Locate every leukocyte (white blood cell).
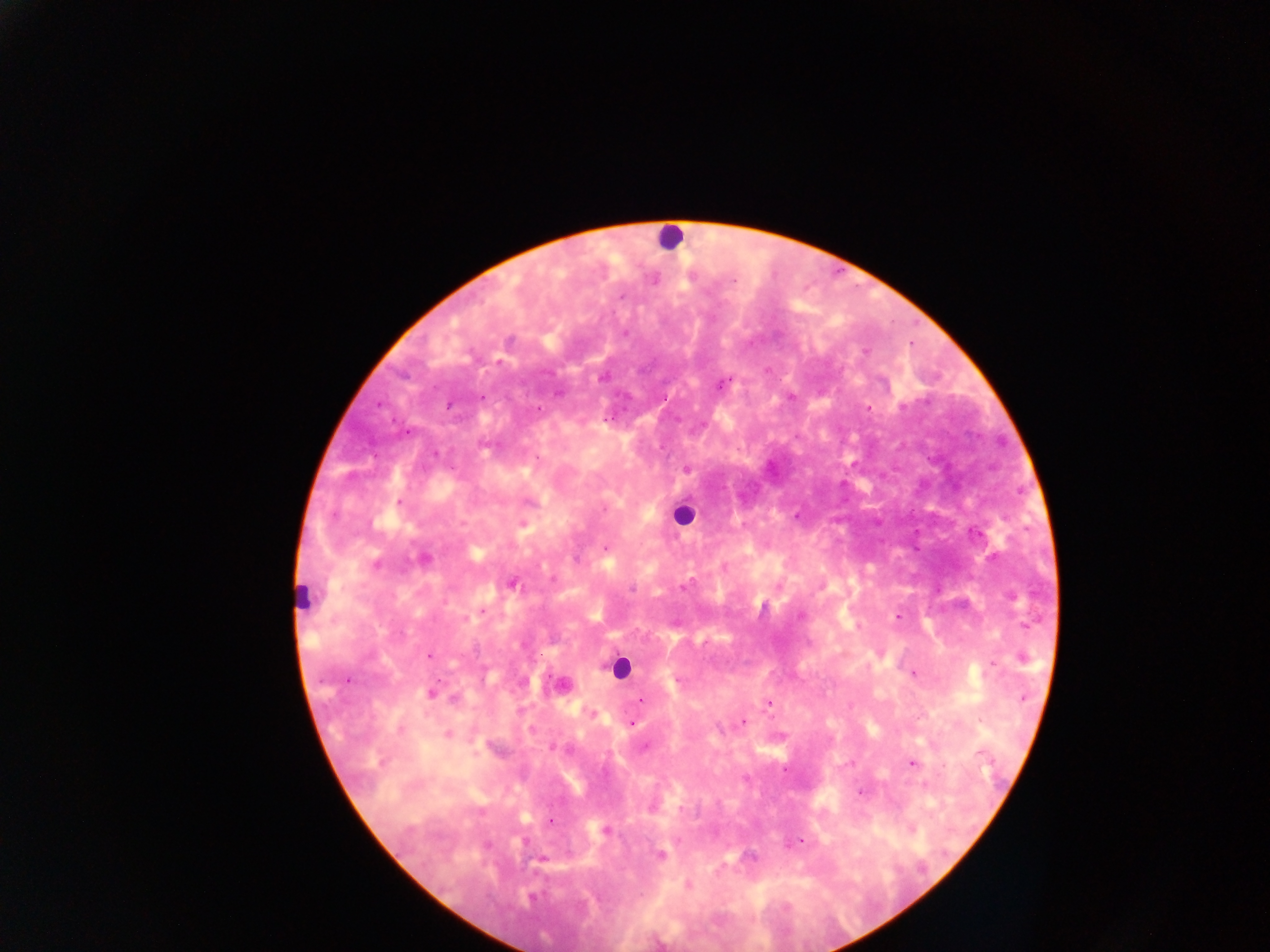
Approximate centers as (x, y) in pixels.
Leukocytes: (668, 237), (685, 515), (302, 597), (620, 668).

capture = mobile-phone photograph through a microscope
country = Ghana
preparation = thick blood smear
malaria parasite locations = approximate centers as (x, y) in pixels: (653, 279), (733, 280), (865, 351), (602, 376), (723, 382), (790, 396), (868, 408), (686, 468), (398, 502), (522, 523), (605, 548), (424, 559), (375, 563), (724, 566), (512, 583), (631, 589), (800, 614), (898, 616), (430, 655), (1021, 656), (914, 673), (347, 679), (563, 684), (431, 693), (639, 701), (768, 702), (591, 713), (743, 720), (631, 723), (447, 735), (551, 747), (912, 762), (861, 791), (652, 806), (551, 820), (910, 829), (605, 830), (799, 840), (660, 854), (750, 857), (541, 859), (686, 884)
field of view = single
image size = 1270×952 pixels